Report the malaria status of this cell.
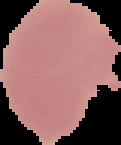
It is uninfected.

Summary:
  - Preparation: thin blood smear
  - Image size: 121×145 pixels
  - Image type: cell region segmented out of the field of view; surrounding area masked to black